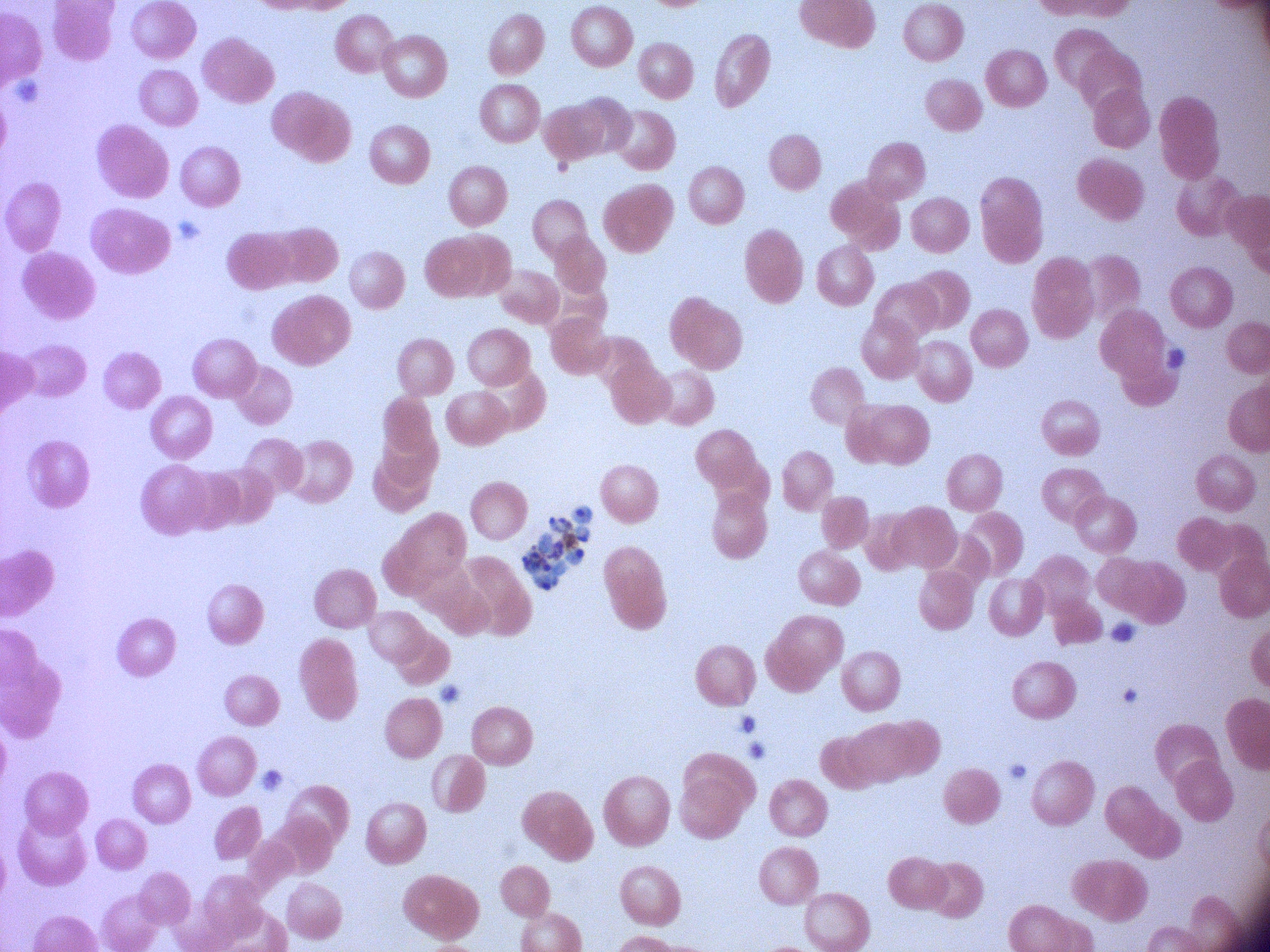

preparation = thin blood smear
schizont locations = approximate bounding boxes as (x1,y1)-(x2,y2) corner pairs in pixels, from the source annotation, which is not necessarily exhaustive: (522,506)-(593,591)
microscope = Leica DM2000 with built-in camera
image size = 1270×952 pixels
species = Plasmodium falciparum
magnification = 100x
field of view = one from this slide
stain = Giemsa